Assess this cell for malaria.
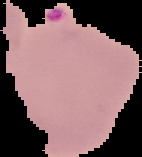
It is parasitized.

From a thin blood film. Image is 142×157 pixels. Segmented cell region on a black background.